Identify the parasite.
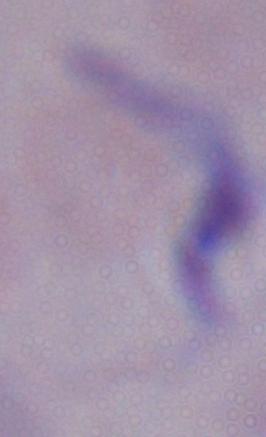
A trypanosome.

magnification: 1000x
modality: photomicrograph